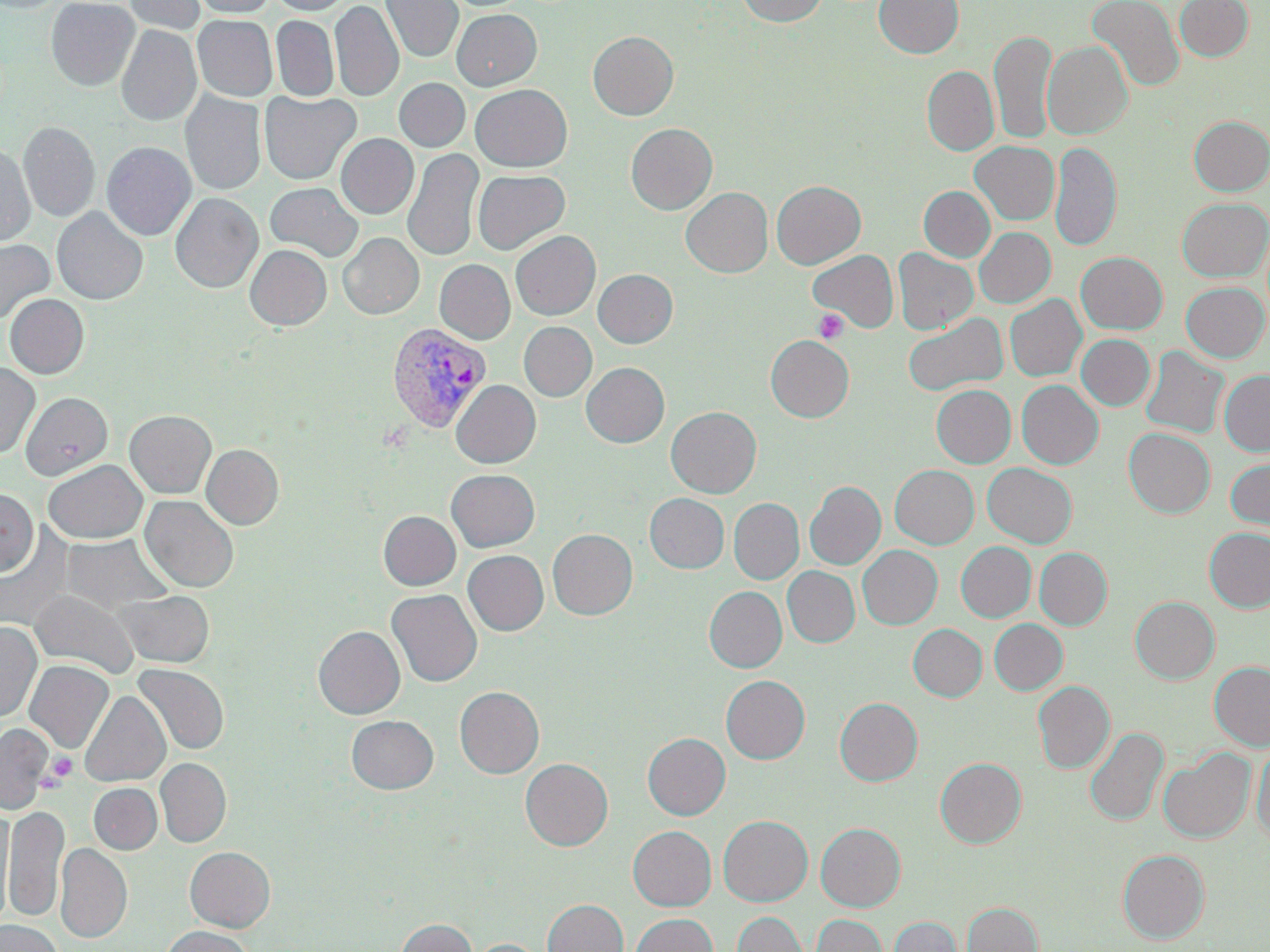

slide-level diagnosis = Plasmodium vivax
field of view = single
Plasmodium vivax-infected red blood cell locations = approximate bounding boxes as (x1, y1, x2, y2) in pixels: (386, 322, 492, 433)
magnification = 1000x
image size = 1270×952 pixels
uninfected red blood cell locations = approximate bounding boxes as (x1, y1, x2, y2) in pixels: (0, 0, 66, 12), (46, 0, 140, 90), (123, 0, 206, 35), (191, 0, 276, 17), (269, 0, 351, 15), (380, 0, 463, 63), (738, 0, 827, 26), (874, 0, 964, 58), (1086, 0, 1184, 92), (1174, 0, 1253, 61), (330, 1, 404, 102), (452, 9, 541, 90), (193, 15, 277, 101), (271, 15, 338, 102), (116, 25, 202, 126), (990, 29, 1056, 145), (588, 31, 678, 120), (1042, 41, 1132, 139), (922, 65, 998, 155), (394, 78, 470, 152), (471, 84, 572, 171), (260, 90, 361, 185), (180, 91, 266, 196), (1188, 116, 1270, 195), (18, 122, 100, 222), (626, 123, 717, 214), (336, 134, 419, 218), (970, 141, 1059, 225), (1050, 141, 1121, 252), (0, 142, 35, 246), (101, 142, 196, 240), (402, 148, 484, 261), (473, 169, 570, 255), (771, 180, 865, 269), (265, 182, 363, 261), (918, 186, 995, 262), (681, 187, 773, 277), (170, 192, 263, 293), (1177, 197, 1269, 282), (52, 208, 147, 305), (974, 228, 1055, 308), (510, 230, 600, 320), (338, 233, 423, 319), (0, 239, 53, 324), (245, 245, 332, 330), (893, 248, 978, 334), (808, 249, 899, 332), (1076, 252, 1167, 334), (434, 259, 515, 344), (593, 269, 678, 348), (1181, 282, 1269, 361), (4, 294, 89, 378), (1005, 294, 1086, 381), (902, 313, 1008, 397), (519, 322, 597, 401), (1076, 334, 1155, 410), (766, 335, 854, 422), (1140, 346, 1229, 438), (0, 362, 40, 458), (581, 362, 669, 447), (1219, 370, 1270, 456), (451, 380, 541, 468), (1016, 380, 1103, 469), (931, 384, 1016, 467), (20, 392, 112, 480), (666, 407, 761, 498), (124, 410, 216, 498), (1124, 428, 1215, 518), (202, 444, 284, 529), (1224, 457, 1270, 535), (43, 460, 147, 543), (983, 463, 1077, 548), (890, 465, 979, 548), (446, 469, 540, 552), (805, 481, 885, 569), (0, 488, 38, 576), (645, 493, 729, 573), (140, 495, 238, 592), (729, 498, 804, 584), (378, 511, 461, 590), (0, 527, 74, 632), (1204, 527, 1270, 612), (548, 528, 637, 620), (61, 534, 170, 614), (956, 542, 1036, 622), (857, 545, 942, 629), (1035, 548, 1112, 630), (463, 550, 548, 635), (782, 567, 860, 647), (704, 586, 787, 672), (386, 589, 482, 686), (29, 590, 138, 677), (115, 590, 214, 667), (1130, 596, 1219, 683), (989, 619, 1067, 694), (0, 622, 41, 722), (908, 624, 987, 701), (313, 626, 405, 719), (24, 660, 114, 754), (1209, 660, 1270, 751), (134, 664, 228, 754), (721, 675, 810, 763), (1033, 681, 1114, 773), (455, 686, 544, 778), (79, 691, 170, 787), (835, 697, 923, 786), (346, 715, 438, 794), (0, 723, 53, 813), (1085, 727, 1168, 826), (643, 733, 730, 820), (1252, 742, 1270, 846), (1158, 748, 1255, 843), (935, 757, 1026, 847), (155, 758, 231, 847), (521, 759, 613, 850), (89, 783, 162, 854), (5, 804, 69, 923), (0, 810, 14, 926), (718, 815, 812, 906), (816, 822, 906, 911), (628, 826, 716, 910), (55, 843, 132, 943), (185, 846, 275, 931), (1118, 849, 1209, 943), (543, 899, 628, 952), (962, 901, 1042, 952), (732, 911, 808, 952), (630, 913, 718, 952), (810, 913, 888, 952), (889, 915, 961, 952), (397, 918, 476, 952), (0, 920, 63, 952), (161, 926, 253, 952), (471, 939, 544, 952)
platelet locations = approximate bounding boxes as (x1, y1, x2, y2) in pixels: (813, 309, 849, 344), (46, 752, 78, 783)
stain = May-Grünwald-Giemsa
modality = optical microscopy
preparation = thin blood smear